Comment on the morphology of the erythrocytes.
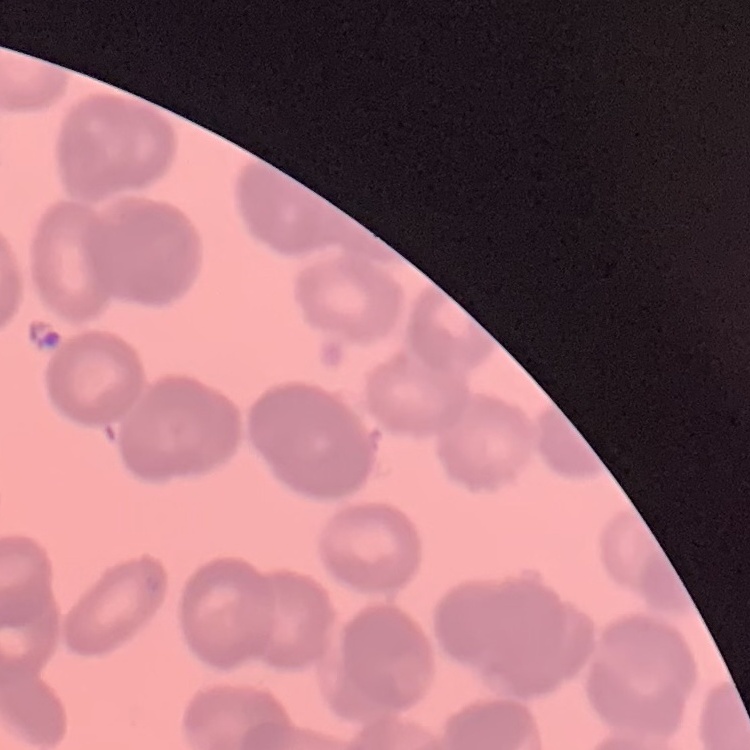

They show rouleaux formation.

Thin blood smear. Field's or Giemsa stain. One tile cut from a larger photomicrograph.